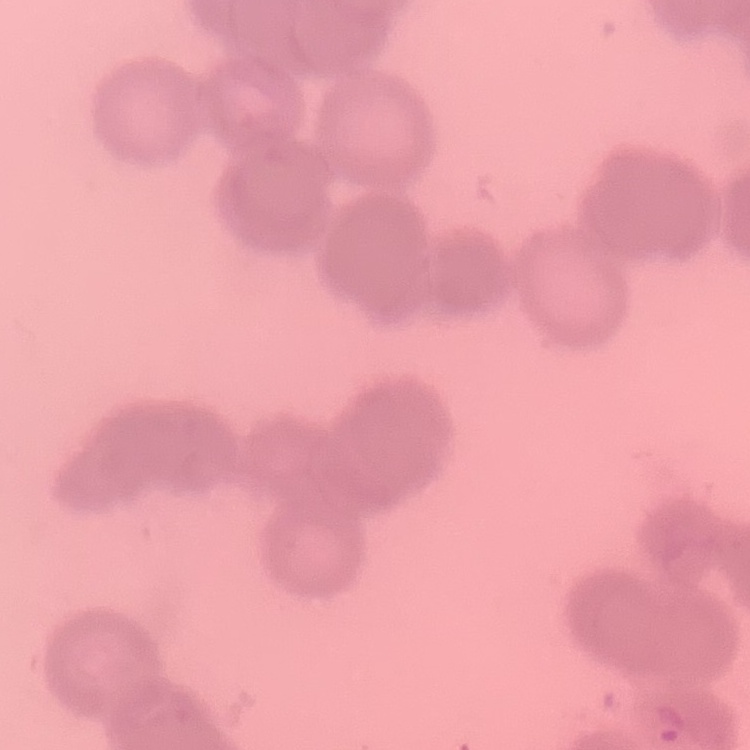
Summary:
  - Red blood cell morphology: rouleaux formation
  - Image type: one tile cut from a larger photomicrograph
  - Preparation: thin peripheral smear
  - Stain: Field's or Giemsa